Classify this cell by malaria status.
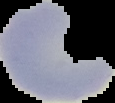
It is uninfected.

From a thin blood film. Image is 115×103 pixels. Segmented cell region on a black background.